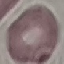 Malaria status: uninfected. Cell patch, automatically extracted from a larger field of view and resized to 64 × 64 pixels. Thin blood smear. Photographed with a smartphone camera at the microscope eyepiece. Giemsa stain.